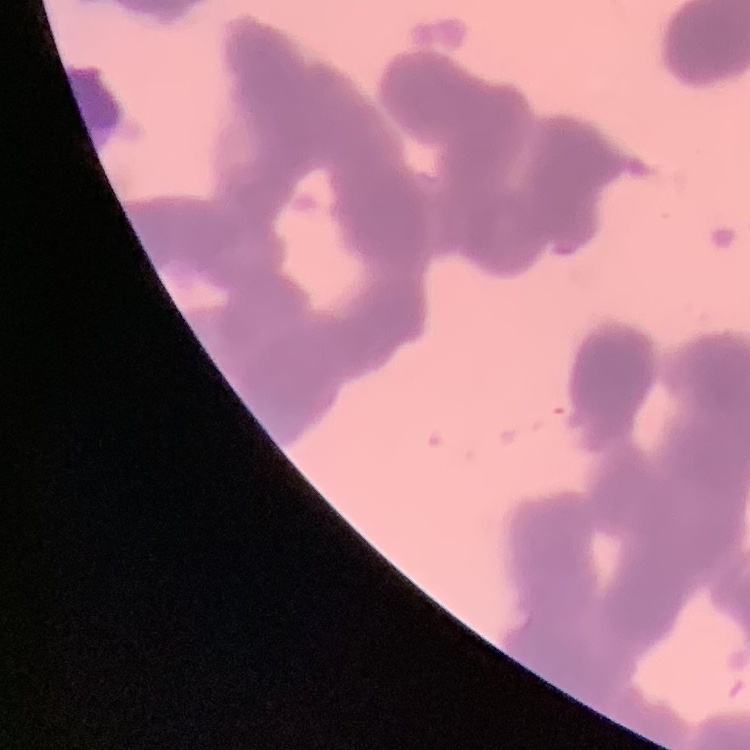

erythrocyte morphology = rouleaux formation
stain = Field's or Giemsa
image type = square crop of a larger photomicrograph
preparation = thin blood film